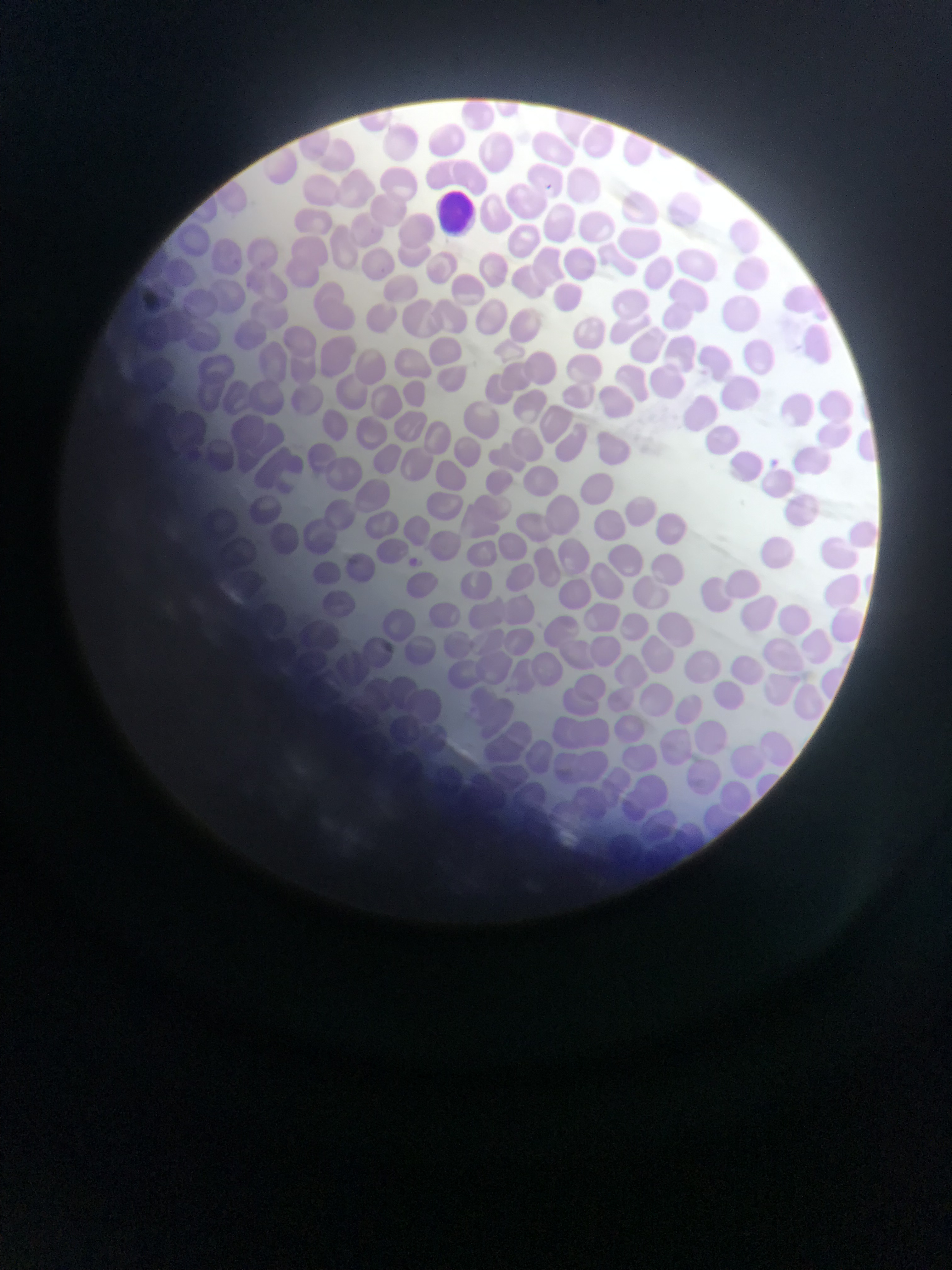
Approximate bounding boxes as [left, top, right, bottom] in pixels. Leukocyte locations: [425, 184, 488, 234]. Mobile-phone photograph taken through the microscope. Collected in Ghana. Thin blood smear. One field of view. Image is 952×1270 pixels.